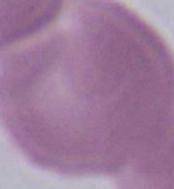
Summary:
  - Identification: red blood cell
  - Modality: micrograph
  - Magnification: 1000x